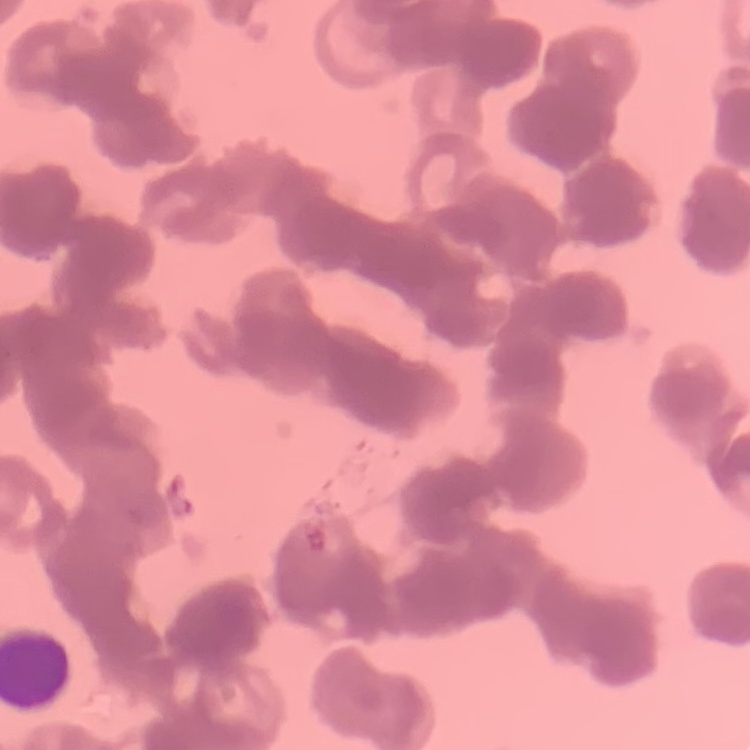

erythrocyte morphology = rouleaux formation
preparation = thin peripheral smear
image type = square crop of a larger photomicrograph
stain = Field's or Giemsa